Identify the preparation type.
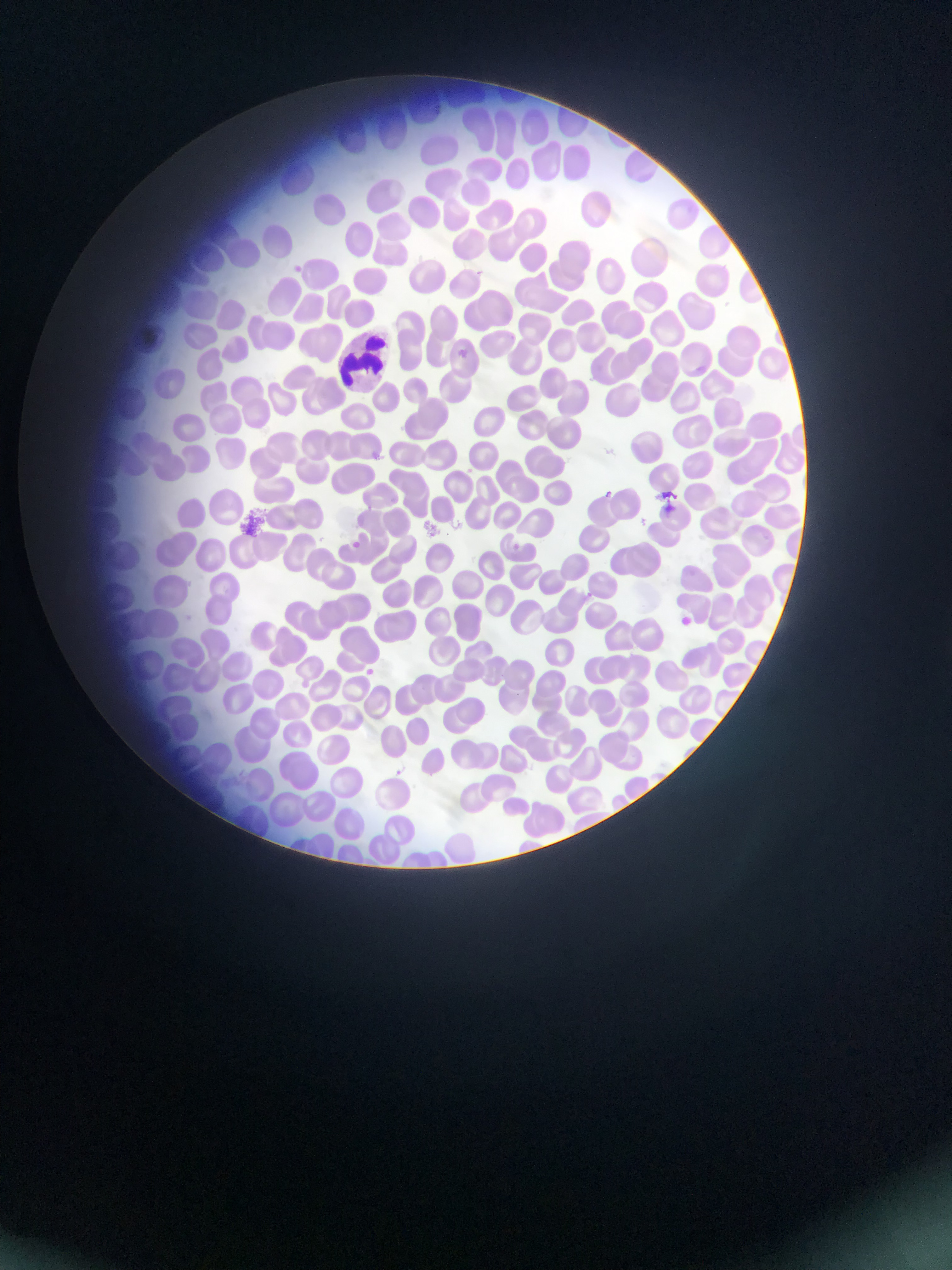

This is a thin smear.

Approximate bounding boxes as (left, top, right, bottom) in pixels. Artifact (stain precipitate or debris) locations: (239, 508, 273, 534). Malaria parasite locations: (454, 345, 471, 361), (601, 487, 616, 500), (655, 491, 681, 515), (349, 536, 365, 551), (506, 539, 523, 554), (584, 587, 598, 601), (676, 615, 693, 629), (362, 665, 378, 679), (396, 765, 409, 777). Leukocyte locations: (342, 332, 394, 388). Photographed through a microscope with a mobile-phone camera. Image is 952×1270 pixels. One field of view. Sample from Ghana.